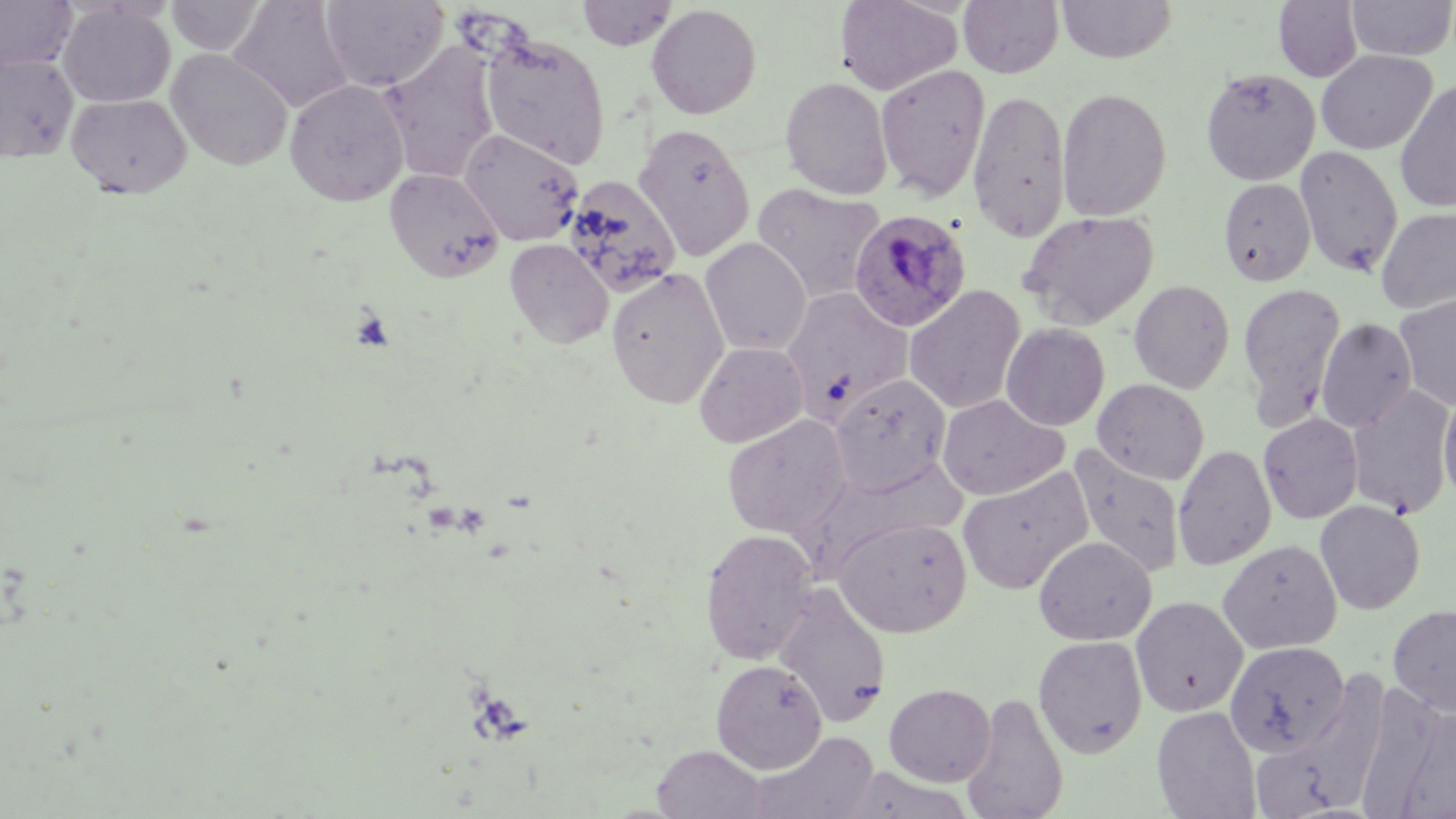 Approximate bounding boxes as [x1, y1, x2, y2] in pixels. Plasmodium ovale-infected red blood cell locations: [847, 209, 972, 333]. Uninfected red blood cell locations: [0, 0, 78, 73], [165, 0, 267, 56], [228, 0, 354, 113], [321, 0, 449, 92], [577, 0, 678, 51], [835, 0, 962, 95], [958, 0, 1063, 78], [1056, 0, 1177, 63], [1274, 0, 1363, 82], [1346, 0, 1455, 61], [58, 3, 175, 108], [646, 4, 762, 119], [479, 31, 611, 169], [380, 44, 500, 183], [166, 48, 293, 171], [1316, 50, 1436, 154], [0, 54, 78, 163], [875, 64, 991, 200], [1200, 67, 1320, 185], [780, 76, 892, 199], [284, 79, 409, 206], [1394, 79, 1456, 214], [1057, 87, 1172, 221], [967, 89, 1071, 241], [66, 93, 191, 198], [633, 123, 755, 261], [459, 129, 584, 246], [1295, 145, 1404, 278], [384, 167, 505, 283], [562, 174, 682, 298], [1217, 177, 1316, 287], [752, 182, 886, 304], [1376, 206, 1456, 314], [1019, 210, 1159, 329], [700, 237, 810, 357], [505, 239, 613, 349], [606, 267, 729, 408], [1128, 280, 1235, 394], [1238, 282, 1346, 427], [904, 285, 1026, 415], [781, 288, 912, 423], [1394, 292, 1456, 413], [1316, 317, 1417, 432], [1000, 323, 1110, 431], [694, 341, 808, 448], [830, 374, 951, 495], [1092, 378, 1209, 485], [1346, 385, 1455, 519], [1439, 391, 1456, 507], [936, 394, 1069, 500], [722, 413, 852, 540], [1258, 413, 1363, 524], [1172, 443, 1277, 570], [1069, 446, 1186, 577], [957, 467, 1093, 594], [1315, 499, 1426, 615], [833, 516, 972, 637], [699, 527, 819, 665], [1033, 535, 1156, 645], [1217, 538, 1342, 654], [773, 584, 892, 728], [1131, 596, 1248, 717], [1388, 603, 1456, 718], [1033, 635, 1148, 758], [1225, 641, 1350, 756], [710, 659, 827, 773], [884, 682, 995, 786], [960, 691, 1069, 819], [1152, 705, 1260, 818], [1393, 705, 1456, 819], [750, 730, 879, 819], [1251, 736, 1355, 817], [652, 744, 768, 818], [839, 766, 974, 819]. Slide-level diagnosis: Plasmodium ovale. Captured at 1000x magnification. Optical microscopy. Image is 1456×819 pixels. Thin blood smear. May-Grünwald-Giemsa stain. Single field of view.